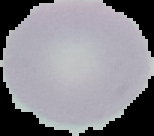 From a thin blood smear. Segmented cell region on a black background. Image is 154×136 pixels. Result: no Plasmodium parasites seen.